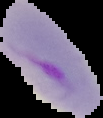
image_type: segmented cell region on a black background
image_size: 103×118 pixels
preparation: thin blood film
result: malaria parasites detected